Locate every malaria parasite.
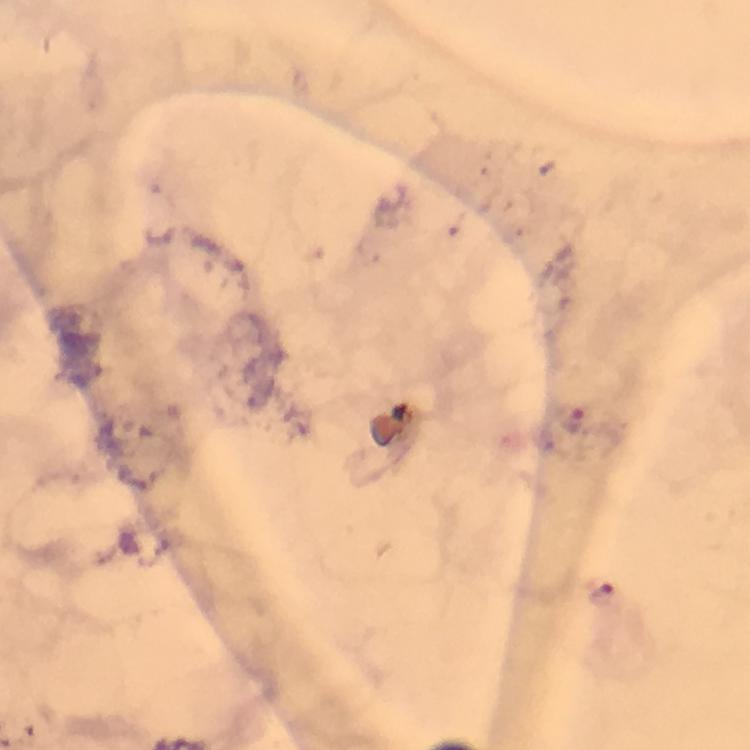

Approximate centers as (x, y) in pixels.
Malaria parasites: (571, 422), (600, 597).

Summary:
  - Immersion oil: applied
  - Preparation: thick blood smear
  - Capture: smartphone photograph through a microscope
  - Stain: Giemsa
  - Cropped from: one field of view
  - Magnification: 100x
  - Image size: 750×750 pixels
  - Context: from a malaria diagnostic workup